Locate every blood parasite and identify its species.
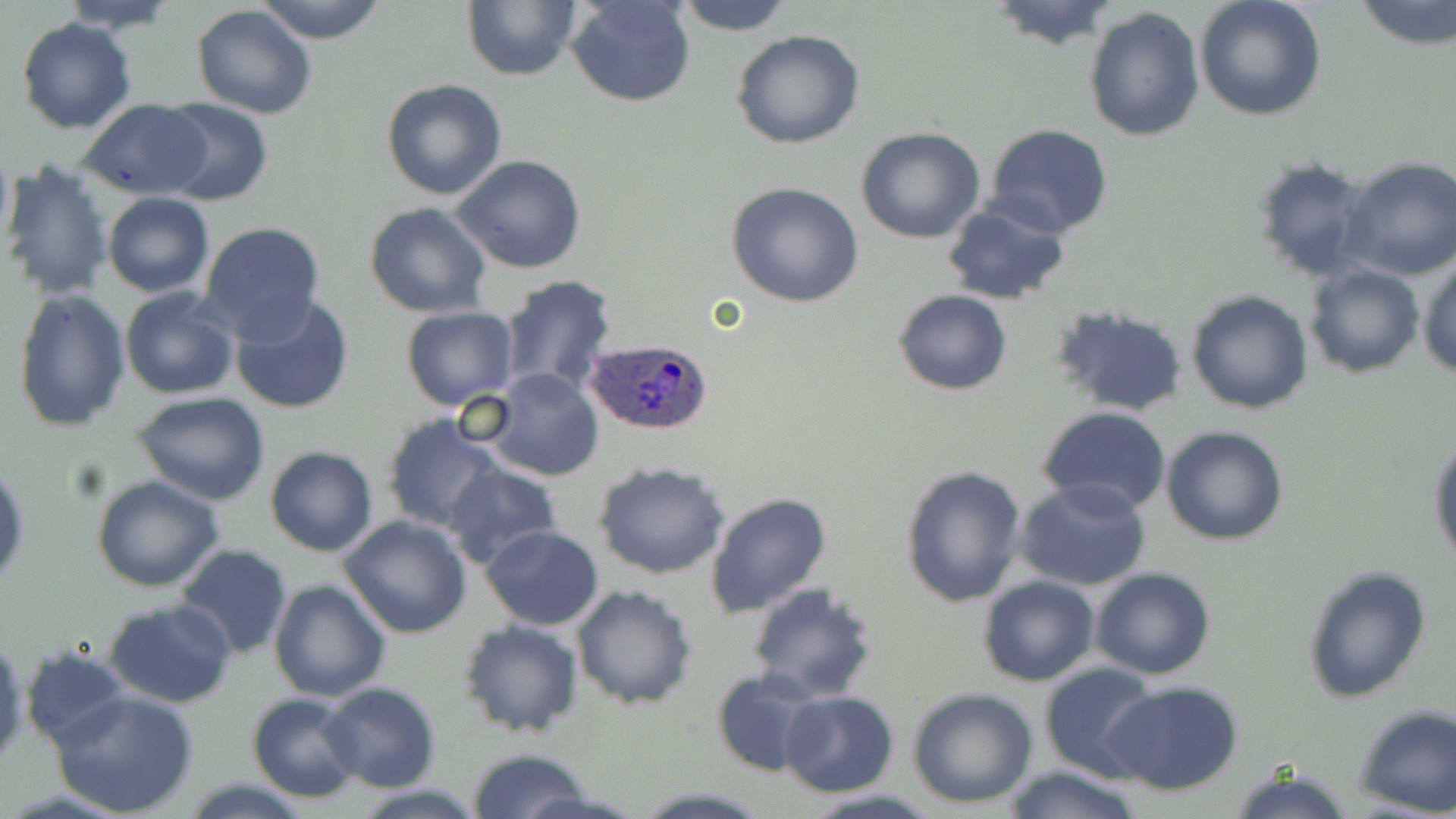
Approximate bounding boxes as named x1/y1/x2/y2 corners in pixels.
Plasmodium ovale-infected red blood cells: (x1=586, y1=339, x2=712, y2=437).
No Plasmodium falciparum, Plasmodium malariae, Plasmodium vivax, Babesia divergens, or Trypanosoma brucei observed.

Summary:
  - Uninfected red blood cell locations: (x1=66, y1=0, x2=175, y2=33), (x1=254, y1=0, x2=389, y2=43), (x1=567, y1=0, x2=695, y2=107), (x1=672, y1=0, x2=797, y2=36), (x1=1194, y1=0, x2=1327, y2=121), (x1=1352, y1=0, x2=1456, y2=48), (x1=986, y1=1, x2=1118, y2=49), (x1=462, y1=2, x2=581, y2=81), (x1=191, y1=3, x2=317, y2=119), (x1=1083, y1=6, x2=1205, y2=143), (x1=14, y1=16, x2=137, y2=134), (x1=731, y1=29, x2=866, y2=150), (x1=380, y1=80, x2=507, y2=201), (x1=78, y1=99, x2=210, y2=199), (x1=157, y1=99, x2=272, y2=205), (x1=984, y1=125, x2=1114, y2=238), (x1=855, y1=126, x2=984, y2=243), (x1=0, y1=143, x2=14, y2=253), (x1=452, y1=155, x2=588, y2=274), (x1=1251, y1=156, x2=1375, y2=282), (x1=1338, y1=158, x2=1456, y2=281), (x1=4, y1=161, x2=113, y2=299), (x1=726, y1=182, x2=864, y2=307), (x1=102, y1=191, x2=214, y2=297), (x1=363, y1=201, x2=491, y2=317), (x1=941, y1=201, x2=1071, y2=306), (x1=198, y1=222, x2=327, y2=343), (x1=1418, y1=256, x2=1456, y2=380), (x1=1305, y1=263, x2=1426, y2=379), (x1=495, y1=274, x2=619, y2=395), (x1=119, y1=287, x2=241, y2=399), (x1=11, y1=288, x2=130, y2=434), (x1=894, y1=289, x2=1012, y2=396), (x1=1187, y1=289, x2=1313, y2=413), (x1=229, y1=294, x2=355, y2=415), (x1=1050, y1=305, x2=1188, y2=418), (x1=400, y1=307, x2=519, y2=410), (x1=483, y1=367, x2=605, y2=482), (x1=132, y1=391, x2=271, y2=505), (x1=1036, y1=407, x2=1171, y2=516), (x1=111, y1=410, x2=254, y2=563), (x1=384, y1=415, x2=509, y2=533), (x1=1161, y1=425, x2=1288, y2=547), (x1=1427, y1=431, x2=1456, y2=570), (x1=265, y1=445, x2=378, y2=556), (x1=593, y1=461, x2=733, y2=580), (x1=442, y1=463, x2=563, y2=571), (x1=0, y1=464, x2=28, y2=592), (x1=899, y1=464, x2=1027, y2=608), (x1=91, y1=475, x2=224, y2=591), (x1=1014, y1=479, x2=1151, y2=590), (x1=704, y1=492, x2=832, y2=619), (x1=338, y1=515, x2=472, y2=640), (x1=480, y1=525, x2=603, y2=630), (x1=174, y1=545, x2=292, y2=660), (x1=1303, y1=565, x2=1433, y2=704), (x1=1090, y1=567, x2=1215, y2=680), (x1=977, y1=574, x2=1100, y2=685), (x1=269, y1=579, x2=390, y2=702), (x1=746, y1=581, x2=879, y2=701), (x1=572, y1=583, x2=698, y2=710), (x1=103, y1=599, x2=236, y2=708), (x1=457, y1=619, x2=583, y2=738), (x1=0, y1=635, x2=28, y2=767), (x1=21, y1=646, x2=132, y2=751), (x1=1040, y1=663, x2=1162, y2=781), (x1=710, y1=668, x2=822, y2=777), (x1=1103, y1=679, x2=1246, y2=795), (x1=320, y1=682, x2=441, y2=791), (x1=907, y1=688, x2=1039, y2=808), (x1=51, y1=689, x2=199, y2=816), (x1=780, y1=690, x2=900, y2=797), (x1=245, y1=691, x2=363, y2=801), (x1=1354, y1=705, x2=1455, y2=816), (x1=468, y1=748, x2=592, y2=819), (x1=1002, y1=764, x2=1142, y2=819), (x1=1228, y1=764, x2=1353, y2=819), (x1=182, y1=779, x2=311, y2=817), (x1=351, y1=785, x2=488, y2=818), (x1=634, y1=787, x2=771, y2=818), (x1=797, y1=788, x2=942, y2=819)
  - Slide-level diagnosis: Plasmodium ovale
  - Image size: 1456×819 pixels
  - Modality: light microscopy
  - Magnification: 1000x
  - Preparation: thin blood film
  - Field of view: single
  - Stain: May-Grünwald-Giemsa